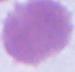

A red blood cell is seen. Captured at 1000x magnification. Micrograph.